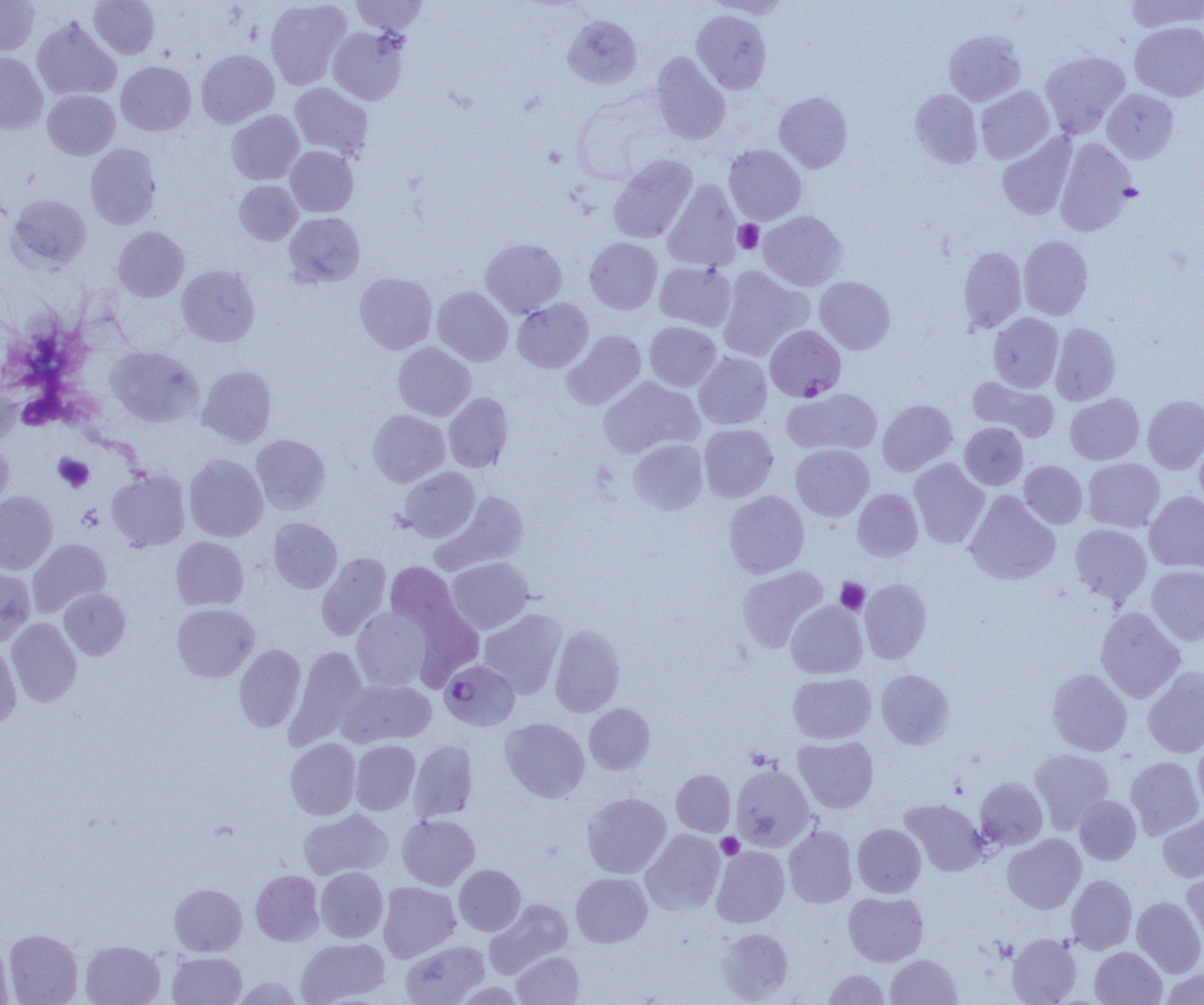

Summary:
  - Coordinate format: approximate bounding boxes as (x1, y1, x2, y2) in pixels
  - Plasmodium falciparum-infected red blood cell locations: (765, 325, 846, 401), (440, 660, 520, 731)
  - Platelet locations: (734, 220, 763, 254), (18, 391, 60, 430), (54, 454, 93, 492), (836, 578, 870, 614), (716, 833, 743, 859)
  - Uninfected red blood cell locations: (0, 0, 40, 55), (89, 0, 160, 59), (265, 0, 352, 89), (351, 0, 428, 35), (706, 0, 793, 18), (1124, 0, 1203, 32), (692, 10, 772, 93), (563, 15, 642, 89), (31, 16, 121, 101), (1130, 21, 1204, 101), (327, 26, 409, 105), (943, 30, 1026, 105), (195, 49, 279, 128), (1040, 51, 1130, 138), (0, 52, 48, 134), (650, 52, 730, 145), (116, 61, 196, 135), (289, 83, 373, 159), (976, 86, 1054, 163), (1102, 88, 1179, 164), (42, 89, 120, 159), (909, 89, 983, 168), (774, 91, 853, 173), (226, 110, 304, 184), (997, 134, 1076, 220), (1055, 138, 1137, 236), (86, 143, 161, 229), (724, 144, 806, 224), (285, 146, 358, 217), (608, 155, 697, 244), (234, 180, 302, 245), (662, 180, 742, 271), (8, 194, 91, 271), (284, 211, 364, 287), (758, 211, 847, 291), (113, 226, 189, 302), (1018, 235, 1093, 320), (480, 237, 567, 317), (585, 237, 663, 314), (958, 247, 1027, 333), (654, 261, 736, 331), (177, 265, 260, 347), (717, 266, 813, 361), (354, 272, 437, 354), (815, 276, 895, 354), (432, 286, 513, 366), (512, 298, 593, 372), (988, 312, 1064, 392), (644, 321, 720, 391), (1050, 322, 1120, 405), (562, 330, 645, 410), (392, 342, 476, 420), (106, 346, 203, 427), (694, 352, 771, 429), (197, 365, 277, 447), (598, 376, 703, 458), (968, 376, 1059, 442), (0, 377, 21, 444), (782, 388, 882, 455), (444, 392, 514, 472), (1065, 393, 1144, 465), (1143, 395, 1204, 474), (877, 399, 957, 475), (368, 409, 449, 487), (960, 422, 1028, 490), (699, 423, 778, 502), (1194, 433, 1204, 513), (251, 434, 331, 514), (628, 438, 708, 514), (0, 440, 13, 513), (791, 444, 874, 520), (184, 454, 268, 541), (909, 458, 989, 548), (1083, 458, 1164, 532), (1019, 461, 1087, 528), (398, 467, 480, 542), (107, 468, 190, 551), (852, 488, 923, 561), (965, 490, 1060, 585), (0, 491, 57, 574), (435, 491, 530, 573), (724, 491, 810, 578), (1145, 491, 1204, 573), (268, 517, 342, 593), (1070, 524, 1152, 605), (171, 536, 248, 610), (28, 539, 111, 616), (316, 553, 392, 641), (446, 557, 534, 634), (385, 561, 465, 639), (736, 565, 828, 653), (1147, 565, 1204, 645), (0, 567, 35, 646), (860, 578, 932, 664), (59, 588, 130, 660), (786, 601, 868, 679), (172, 603, 258, 682), (1095, 606, 1185, 703), (351, 607, 432, 691), (478, 609, 566, 699), (6, 618, 82, 707), (549, 624, 625, 717), (0, 640, 21, 729), (234, 644, 305, 732), (286, 646, 367, 749), (1143, 666, 1204, 758), (1047, 668, 1132, 756), (876, 669, 954, 749), (788, 672, 876, 744), (338, 677, 436, 748), (584, 703, 655, 774), (500, 717, 590, 803), (794, 736, 878, 812), (1193, 737, 1204, 814), (285, 738, 360, 820), (350, 740, 420, 814), (409, 740, 478, 821), (1030, 748, 1115, 833), (1125, 756, 1203, 839), (730, 763, 815, 852), (671, 769, 735, 836), (975, 777, 1048, 849), (582, 792, 671, 878), (1074, 796, 1141, 865), (901, 799, 989, 876), (298, 809, 393, 880), (1158, 812, 1204, 882), (397, 814, 480, 890), (852, 823, 926, 897), (783, 825, 857, 908), (642, 829, 725, 915), (1003, 834, 1086, 913), (711, 845, 789, 928), (454, 864, 525, 935), (1182, 866, 1204, 947), (315, 867, 388, 942), (250, 870, 323, 945), (571, 872, 652, 947), (1066, 875, 1137, 953), (378, 882, 460, 962), (169, 883, 247, 955), (844, 892, 928, 966), (1132, 896, 1204, 977), (485, 898, 573, 978), (717, 927, 793, 1003), (4, 929, 82, 1005), (1007, 933, 1081, 1004), (0, 935, 13, 1005), (296, 937, 390, 1004), (400, 939, 489, 1005), (80, 940, 165, 1005), (1090, 947, 1166, 1004), (511, 950, 584, 1005), (168, 952, 246, 1005), (885, 954, 962, 1004), (1161, 968, 1204, 1004), (823, 969, 890, 1004), (232, 976, 303, 1004)
  - Slide-level diagnosis: Plasmodium falciparum
  - Magnification: 1000x
  - Preparation: thin blood smear
  - Field of view: one of a larger specimen
  - Modality: optical microscopy
  - Image size: 1204×1005 pixels